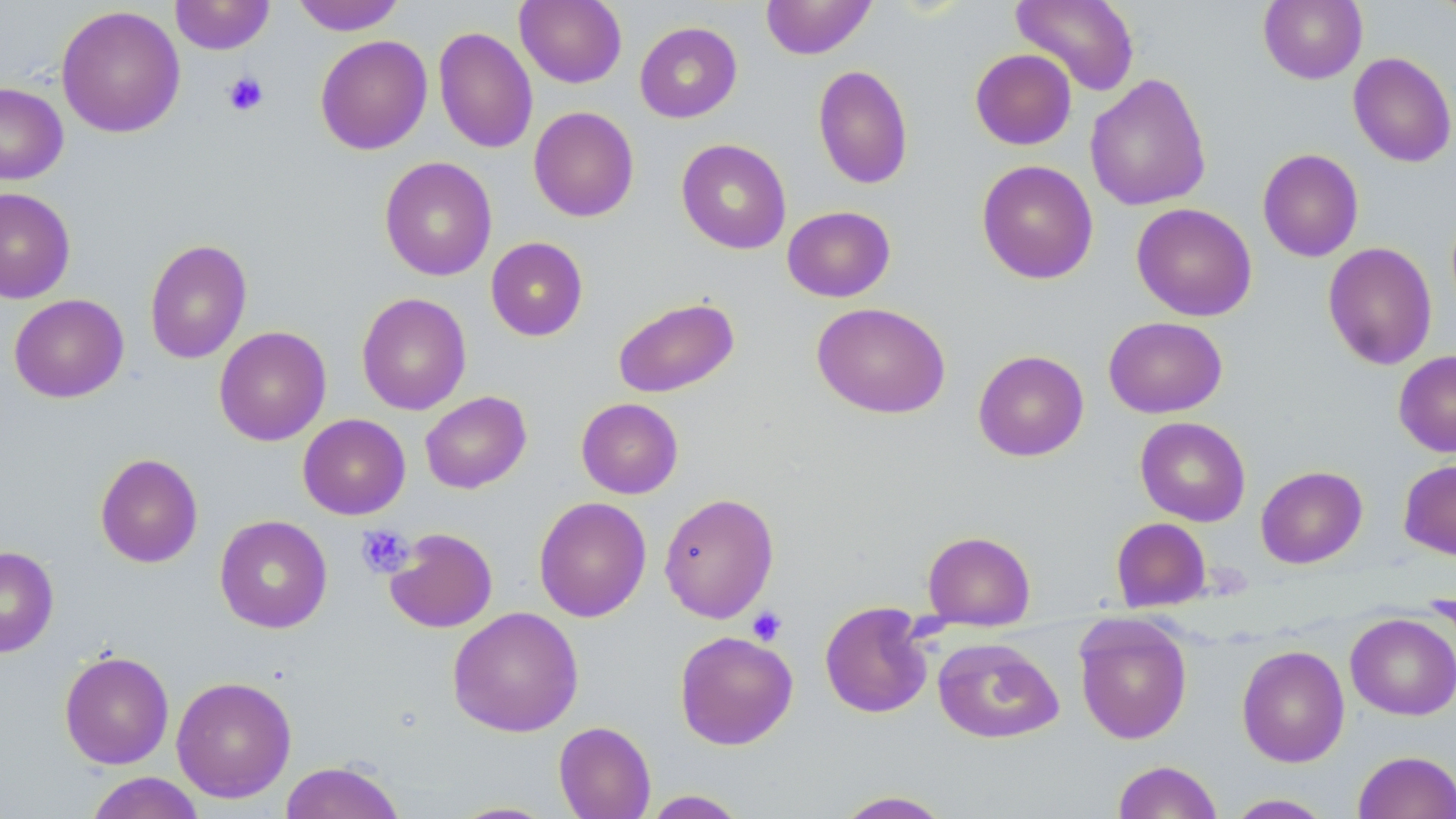 Approximate bounding boxes as named x1/y1/x2/y2 corners in pixels. Platelet locations: (x1=222, y1=71, x2=269, y2=116), (x1=356, y1=524, x2=414, y2=578), (x1=747, y1=606, x2=787, y2=646). Uninfected red blood cell locations: (x1=171, y1=0, x2=274, y2=54), (x1=292, y1=0, x2=405, y2=35), (x1=515, y1=0, x2=627, y2=88), (x1=760, y1=0, x2=877, y2=59), (x1=1011, y1=0, x2=1139, y2=96), (x1=1258, y1=0, x2=1367, y2=84), (x1=56, y1=5, x2=186, y2=138), (x1=635, y1=21, x2=742, y2=123), (x1=433, y1=26, x2=537, y2=154), (x1=315, y1=34, x2=432, y2=155), (x1=970, y1=48, x2=1077, y2=150), (x1=1348, y1=51, x2=1456, y2=168), (x1=813, y1=65, x2=914, y2=190), (x1=1085, y1=73, x2=1212, y2=211), (x1=0, y1=81, x2=68, y2=185), (x1=528, y1=106, x2=639, y2=222), (x1=676, y1=139, x2=791, y2=254), (x1=1257, y1=148, x2=1364, y2=262), (x1=379, y1=156, x2=497, y2=281), (x1=976, y1=159, x2=1098, y2=284), (x1=0, y1=187, x2=75, y2=303), (x1=1131, y1=203, x2=1257, y2=322), (x1=782, y1=205, x2=896, y2=302), (x1=486, y1=237, x2=588, y2=341), (x1=144, y1=238, x2=252, y2=364), (x1=1322, y1=242, x2=1437, y2=370), (x1=356, y1=292, x2=472, y2=415), (x1=9, y1=294, x2=129, y2=403), (x1=612, y1=296, x2=740, y2=398), (x1=812, y1=302, x2=950, y2=419), (x1=1103, y1=316, x2=1227, y2=419), (x1=213, y1=325, x2=331, y2=446), (x1=973, y1=350, x2=1089, y2=461), (x1=1394, y1=351, x2=1456, y2=457), (x1=419, y1=391, x2=532, y2=494), (x1=576, y1=397, x2=683, y2=499), (x1=298, y1=414, x2=410, y2=520), (x1=1135, y1=417, x2=1250, y2=526), (x1=95, y1=452, x2=203, y2=568), (x1=1398, y1=459, x2=1456, y2=560), (x1=1255, y1=466, x2=1368, y2=568), (x1=659, y1=492, x2=779, y2=623), (x1=533, y1=496, x2=652, y2=622), (x1=214, y1=515, x2=333, y2=633), (x1=1111, y1=517, x2=1211, y2=612), (x1=385, y1=527, x2=498, y2=633), (x1=923, y1=530, x2=1035, y2=626), (x1=0, y1=546, x2=59, y2=657), (x1=819, y1=600, x2=934, y2=718), (x1=447, y1=606, x2=584, y2=737), (x1=1345, y1=612, x2=1456, y2=720), (x1=1074, y1=613, x2=1193, y2=745), (x1=674, y1=630, x2=798, y2=750), (x1=932, y1=637, x2=1064, y2=743), (x1=1236, y1=644, x2=1350, y2=767), (x1=59, y1=650, x2=174, y2=769), (x1=171, y1=675, x2=296, y2=803), (x1=553, y1=721, x2=656, y2=819), (x1=1353, y1=750, x2=1456, y2=819), (x1=279, y1=760, x2=406, y2=819), (x1=1111, y1=760, x2=1223, y2=818), (x1=84, y1=772, x2=206, y2=819), (x1=641, y1=790, x2=750, y2=818), (x1=833, y1=790, x2=953, y2=818), (x1=1225, y1=793, x2=1335, y2=818), (x1=447, y1=801, x2=559, y2=818). Slide-level diagnosis: no evidence of blood parasites. Optical microscopy. One field of a larger specimen. Thin blood smear. Image is 1456×819 pixels. May-Grünwald-Giemsa stain. 1000x magnification.